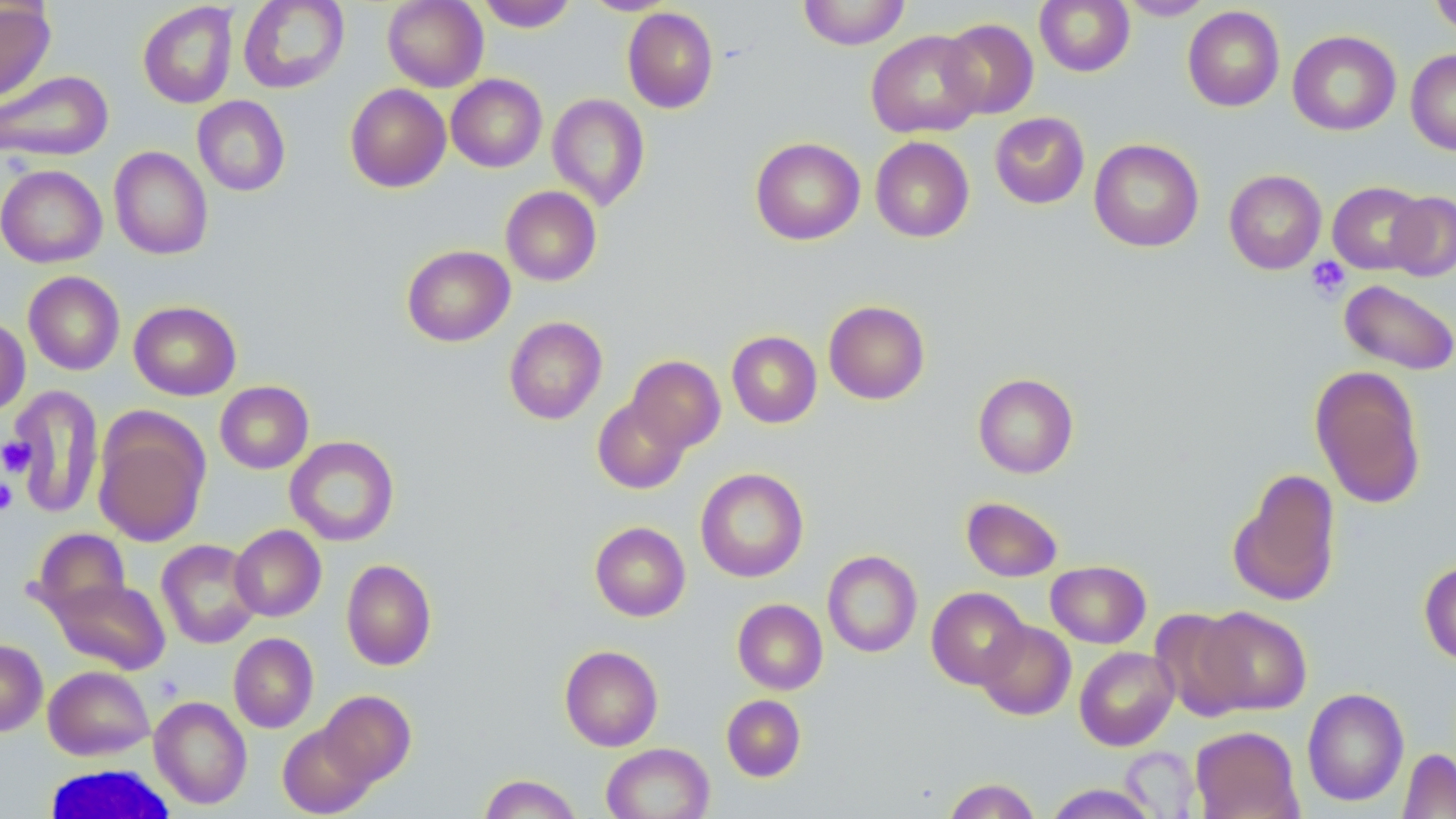
slide-level diagnosis = negative for blood parasites
image size = 1456×819 pixels
field of view = single
uninfected red blood cell locations = approximate bounding boxes as [x1, y1, x2, y2] in pixels: [238, 0, 350, 94], [383, 0, 488, 92], [580, 0, 681, 15], [798, 0, 910, 49], [1034, 0, 1135, 76], [1117, 0, 1215, 20], [1430, 0, 1456, 39], [0, 1, 56, 103], [477, 1, 578, 32], [137, 2, 239, 109], [1183, 6, 1285, 112], [622, 7, 718, 113], [938, 18, 1039, 119], [865, 30, 985, 138], [1288, 30, 1401, 136], [1406, 49, 1456, 156], [0, 70, 113, 162], [446, 74, 547, 172], [345, 84, 451, 192], [547, 94, 650, 210], [192, 96, 291, 196], [989, 112, 1090, 209], [870, 136, 974, 242], [751, 137, 865, 245], [1088, 139, 1204, 252], [109, 146, 212, 260], [1, 165, 107, 268], [1224, 170, 1326, 274], [1327, 181, 1427, 274], [501, 186, 602, 286], [1385, 191, 1456, 281], [402, 244, 515, 346], [23, 271, 125, 375], [1339, 279, 1456, 374], [129, 300, 242, 400], [823, 300, 930, 404], [0, 316, 30, 416], [504, 316, 607, 424], [727, 330, 822, 428], [625, 355, 725, 454], [1309, 366, 1427, 510], [973, 373, 1078, 478], [215, 381, 313, 474], [6, 385, 104, 519], [592, 396, 691, 494], [94, 415, 210, 547], [285, 436, 399, 546], [695, 467, 809, 582], [1228, 469, 1342, 606], [961, 496, 1063, 582], [590, 521, 690, 621], [230, 524, 326, 621], [30, 528, 131, 620], [156, 539, 261, 648], [822, 550, 922, 657], [341, 559, 436, 670], [1046, 560, 1151, 648], [1418, 560, 1456, 665], [53, 578, 170, 674], [926, 587, 1030, 689], [733, 598, 827, 694], [1194, 606, 1312, 715], [1150, 608, 1252, 720], [976, 621, 1076, 720], [228, 632, 319, 733], [0, 639, 47, 736], [559, 645, 663, 751], [1075, 646, 1179, 750], [43, 665, 155, 760], [1302, 687, 1409, 807], [318, 690, 416, 786], [721, 694, 805, 781], [150, 696, 252, 809], [277, 723, 377, 817], [1189, 725, 1304, 819], [601, 743, 715, 819], [1120, 746, 1200, 816], [1398, 748, 1456, 818], [479, 774, 581, 818], [943, 778, 1041, 818], [1043, 784, 1159, 818]
magnification = 1000x
modality = light microscopy
white blood cell locations = approximate bounding boxes as [x1, y1, x2, y2] in pixels: [39, 763, 182, 818]
preparation = thin blood smear
stain = May-Grünwald-Giemsa
platelet locations = approximate bounding boxes as [x1, y1, x2, y2] in pixels: [1306, 257, 1351, 300], [1, 437, 36, 476], [0, 479, 18, 514]